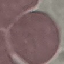

Malaria status: uninfected. Acquired by smartphone through the microscope eyepiece. Cell patch, automatically extracted from a larger field of view and resized to 64 × 64 pixels. Thin blood film. Giemsa-stained preparation.